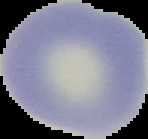
Summary:
  - Preparation: thin blood smear
  - Image size: 148×139 pixels
  - Image type: segmented cell region on a black background
  - Malaria status: uninfected